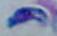
Photomicrograph. 1000x magnification. Toxoplasma gondii is shown.